State the preparation type.
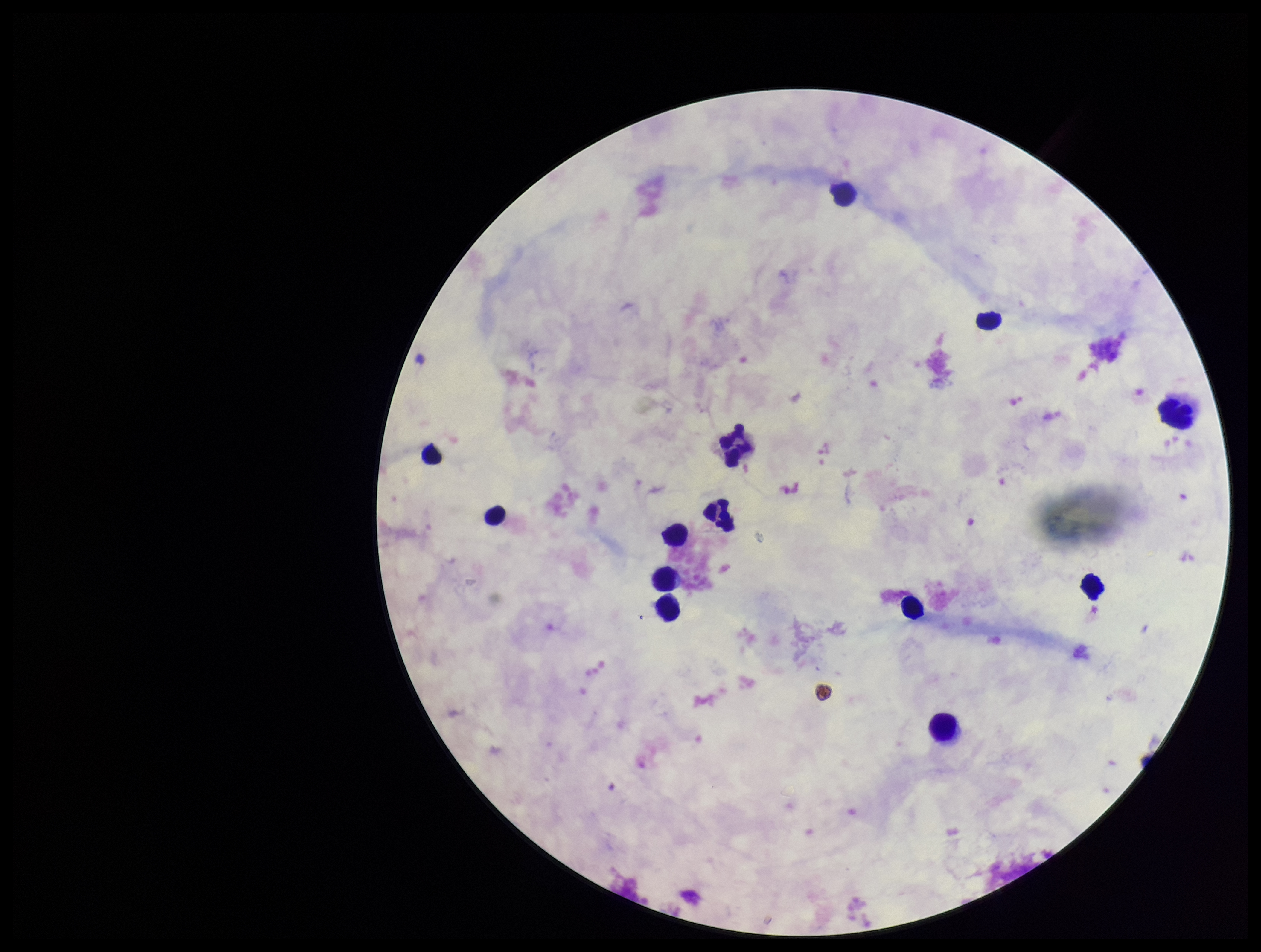
A thick smear.

Parasite count: 0. Stained with Giemsa. Image is 1261×952 pixels. Leukocyte count: 13. Patient malaria status: negative. Plasmodium parasites: none seen. Photographed through the microscope eyepiece with a smartphone camera. One field from this slide.